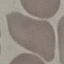

result = negative for malaria parasites
image type = automatically extracted cell patch, resized to 64 × 64 pixels
preparation = thin blood smear
stain = Giemsa
capture = smartphone through the microscope eyepiece